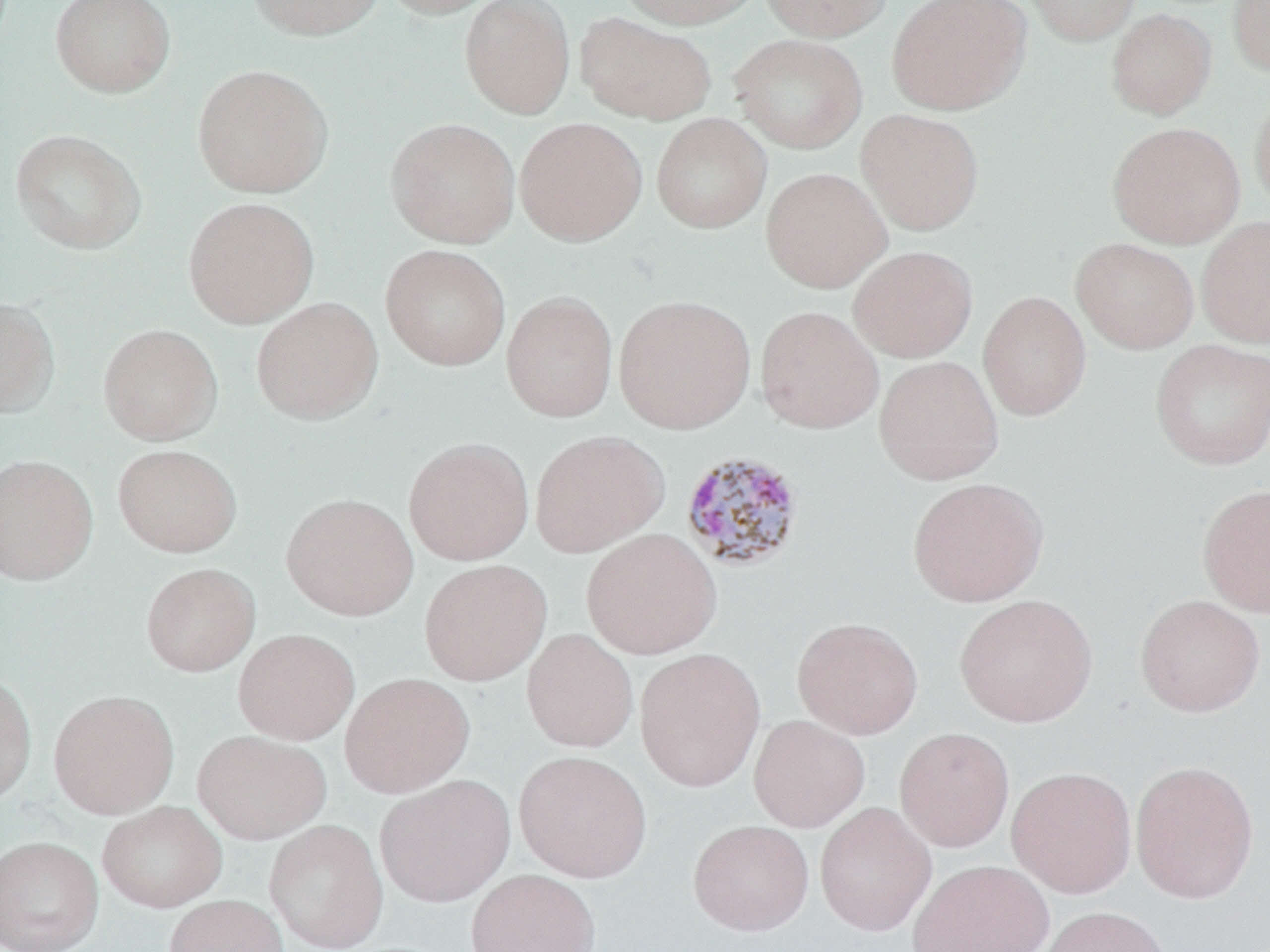
Summary:
  - Coordinate format: approximate bounding boxes as named x1/y1/x2/y2 corners in pixels
  - Uninfected red blood cell locations: (x1=49, y1=0, x2=176, y2=99), (x1=247, y1=0, x2=385, y2=41), (x1=376, y1=0, x2=505, y2=19), (x1=459, y1=0, x2=575, y2=119), (x1=617, y1=0, x2=765, y2=29), (x1=759, y1=0, x2=892, y2=41), (x1=886, y1=0, x2=1032, y2=116), (x1=1021, y1=0, x2=1141, y2=46), (x1=1228, y1=0, x2=1270, y2=77), (x1=1105, y1=8, x2=1217, y2=120), (x1=574, y1=12, x2=717, y2=125), (x1=728, y1=33, x2=868, y2=155), (x1=192, y1=64, x2=333, y2=198), (x1=1250, y1=91, x2=1270, y2=217), (x1=855, y1=109, x2=985, y2=235), (x1=650, y1=113, x2=772, y2=234), (x1=385, y1=117, x2=521, y2=248), (x1=513, y1=117, x2=647, y2=246), (x1=1107, y1=121, x2=1246, y2=249), (x1=10, y1=129, x2=147, y2=255), (x1=760, y1=167, x2=892, y2=293), (x1=182, y1=196, x2=319, y2=329), (x1=1196, y1=215, x2=1270, y2=349), (x1=1070, y1=237, x2=1200, y2=354), (x1=380, y1=244, x2=510, y2=371), (x1=847, y1=245, x2=978, y2=363), (x1=500, y1=290, x2=619, y2=423), (x1=977, y1=290, x2=1092, y2=421), (x1=613, y1=294, x2=756, y2=434), (x1=0, y1=296, x2=61, y2=419), (x1=250, y1=296, x2=384, y2=425), (x1=755, y1=305, x2=884, y2=434), (x1=97, y1=323, x2=224, y2=446), (x1=1149, y1=339, x2=1270, y2=471), (x1=873, y1=355, x2=1004, y2=485), (x1=528, y1=430, x2=669, y2=557), (x1=402, y1=437, x2=534, y2=566), (x1=112, y1=444, x2=242, y2=557), (x1=0, y1=454, x2=99, y2=586), (x1=906, y1=477, x2=1049, y2=607), (x1=1197, y1=483, x2=1270, y2=618), (x1=281, y1=492, x2=418, y2=621), (x1=580, y1=528, x2=722, y2=660), (x1=418, y1=559, x2=552, y2=686), (x1=140, y1=562, x2=260, y2=677), (x1=954, y1=593, x2=1097, y2=728), (x1=1134, y1=594, x2=1266, y2=717), (x1=791, y1=616, x2=923, y2=740), (x1=233, y1=628, x2=360, y2=744), (x1=521, y1=628, x2=638, y2=753), (x1=634, y1=647, x2=766, y2=792), (x1=0, y1=669, x2=37, y2=808), (x1=339, y1=672, x2=475, y2=798), (x1=47, y1=689, x2=179, y2=819), (x1=748, y1=714, x2=871, y2=833), (x1=894, y1=726, x2=1015, y2=852), (x1=192, y1=729, x2=331, y2=844), (x1=514, y1=750, x2=652, y2=883), (x1=1130, y1=759, x2=1259, y2=904), (x1=1006, y1=766, x2=1137, y2=898), (x1=375, y1=774, x2=515, y2=907), (x1=96, y1=800, x2=227, y2=913), (x1=814, y1=801, x2=936, y2=937), (x1=264, y1=819, x2=389, y2=952), (x1=687, y1=819, x2=814, y2=935), (x1=0, y1=835, x2=104, y2=952), (x1=907, y1=859, x2=1054, y2=952), (x1=465, y1=868, x2=602, y2=952), (x1=163, y1=894, x2=290, y2=952), (x1=1036, y1=905, x2=1172, y2=952)
  - Plasmodium malariae-infected red blood cell locations: (x1=680, y1=449, x2=806, y2=572)
  - Slide-level diagnosis: Plasmodium malariae
  - Preparation: thin blood film
  - Field of view: one of a larger specimen
  - Stain: May-Grünwald-Giemsa
  - Magnification: 1000x
  - Image size: 1270×952 pixels
  - Modality: optical microscopy